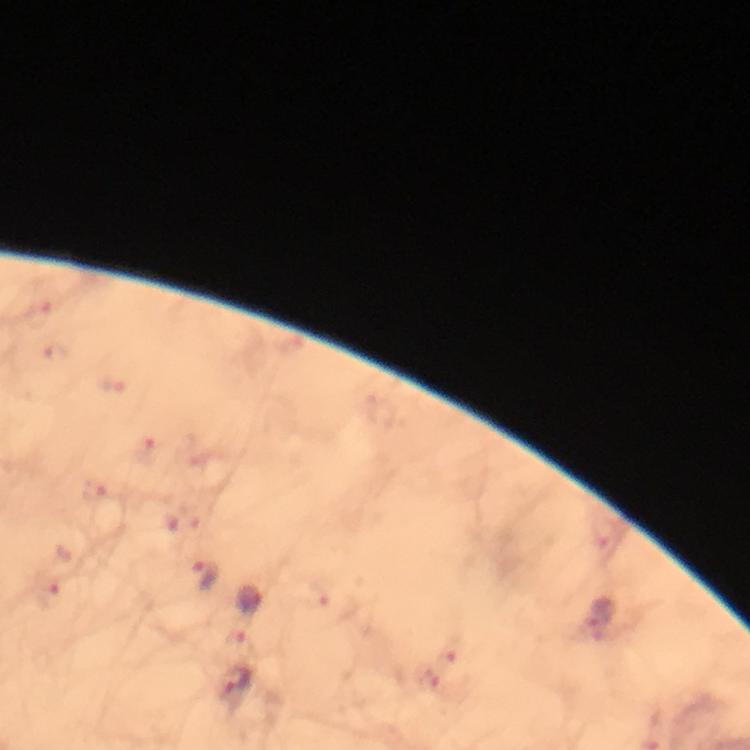

Approximate object centers, in pixels from the top-left corner.
Summary:
  - Plasmodium parasite locations: (x=203, y=576), (x=248, y=599), (x=599, y=617), (x=235, y=683)
  - Context: from a diagnostic examination for malaria
  - Magnification: 100x
  - Stain: Giemsa
  - Capture: smartphone camera through the microscope
  - Cropped from: a single field of view
  - Image size: 750×750 pixels
  - Immersion oil: used
  - Preparation: thick blood film